Identify the parasite.
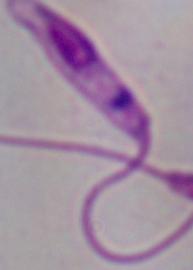
Leishmania.

Micrograph. 1000x magnification.